Report the malaria status of this cell.
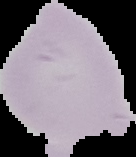

Uninfected.

From a thin blood smear. Cell region segmented out of the field of view; the surrounding area is masked to black. Image is 136×157 pixels.